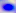
modality = micrograph
identification = Toxoplasma gondii
magnification = 400x